Report the malaria status of this cell.
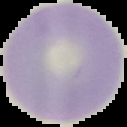

It is uninfected.

Cell region segmented out of the field of view; the surrounding area is masked to black. Image is 127×127 pixels. From a thin blood film.